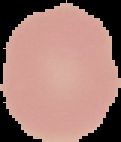

Segmented cell region on a black background. Image is 121×142 pixels. Malaria status: uninfected. From a thin blood smear.